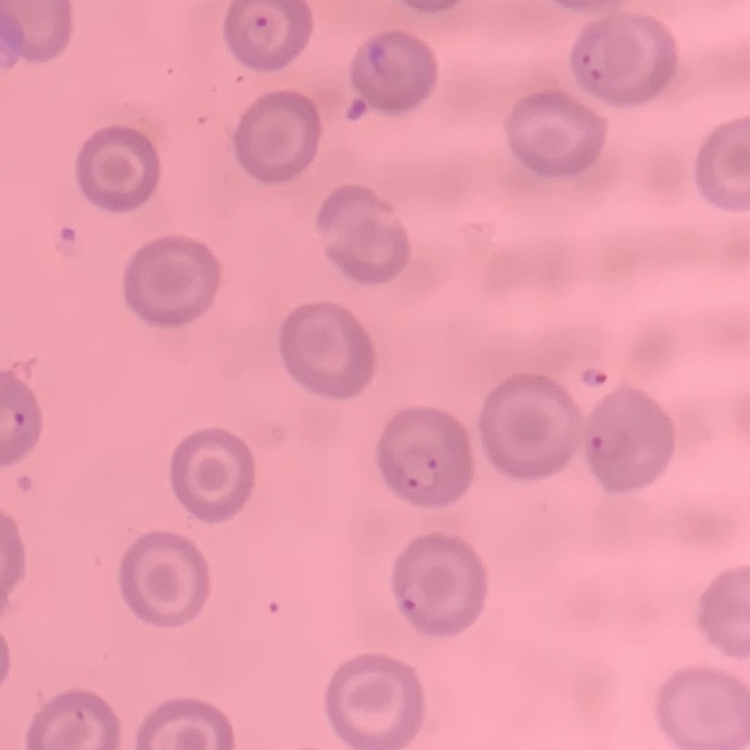

The red blood cells show no rouleaux formation. Thin blood film. Square crop of a larger photomicrograph. Field's or Giemsa stain.